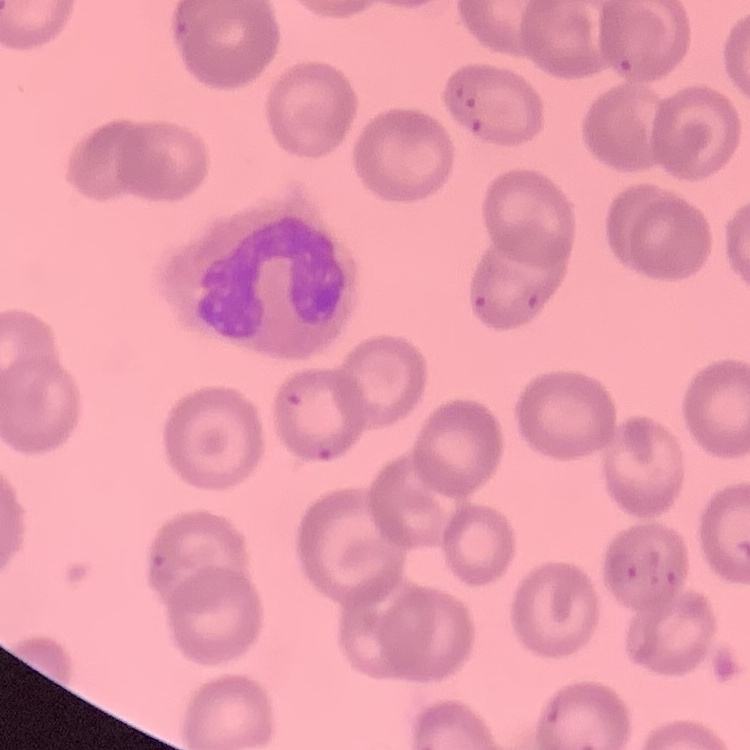
{
  "erythrocyte_morphology": "no rouleaux formation",
  "image_type": "square crop of a larger photomicrograph",
  "preparation": "thin blood film",
  "stain": "Field's or Giemsa"
}